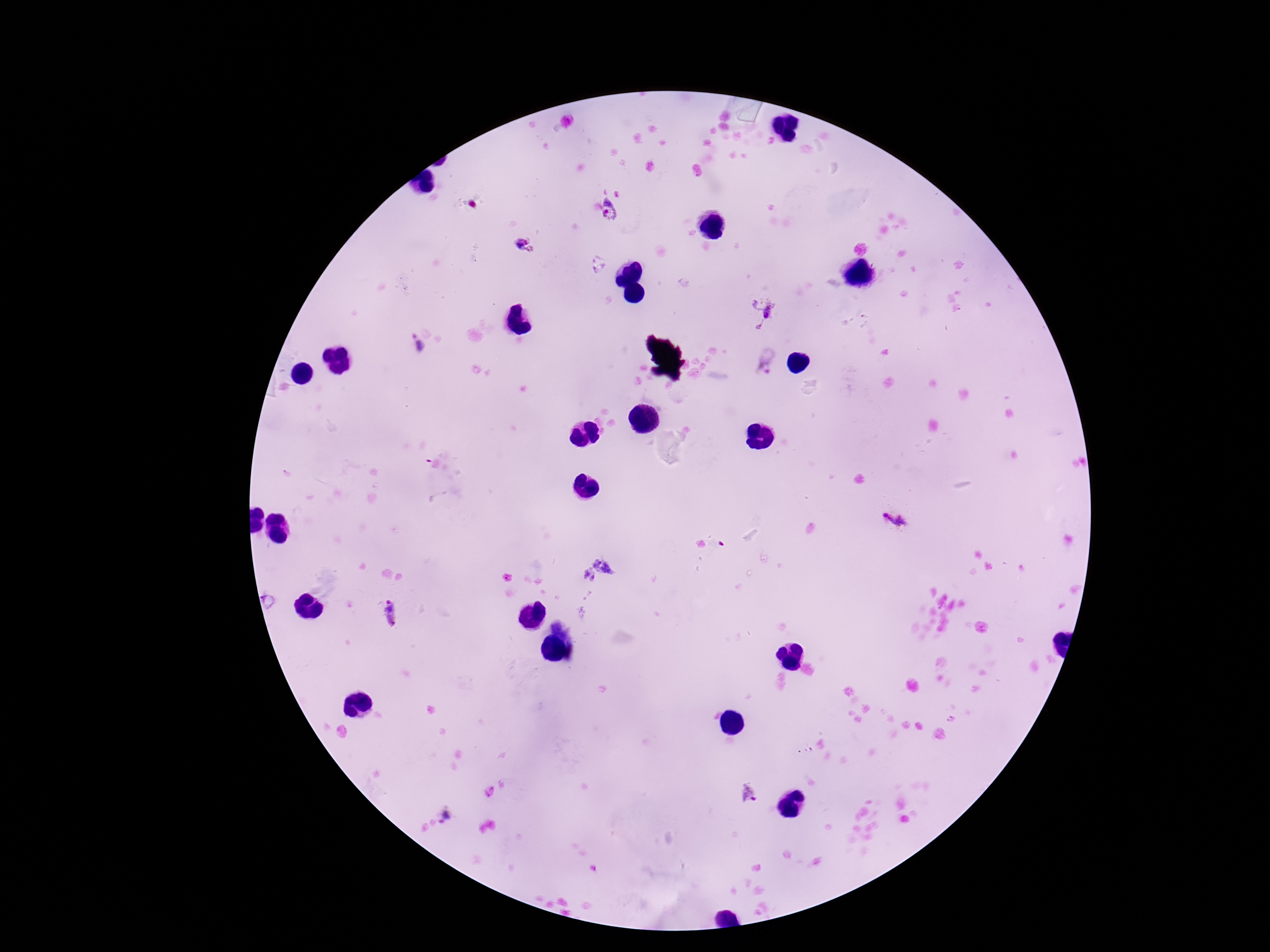

Approximate centers as {x, y} in pixels. Plasmodium parasite locations: {611, 212}, {523, 245}, {762, 313}, {418, 346}, {766, 362}, {894, 517}, {597, 573}, {393, 615}, {745, 794}, {448, 818}. Giemsa stain. Patient malaria status: infected. 100x magnification. Thick blood smear. Image is 1270×952 pixels. Photographed through the microscope eyepiece with a smartphone camera. Single field of view.